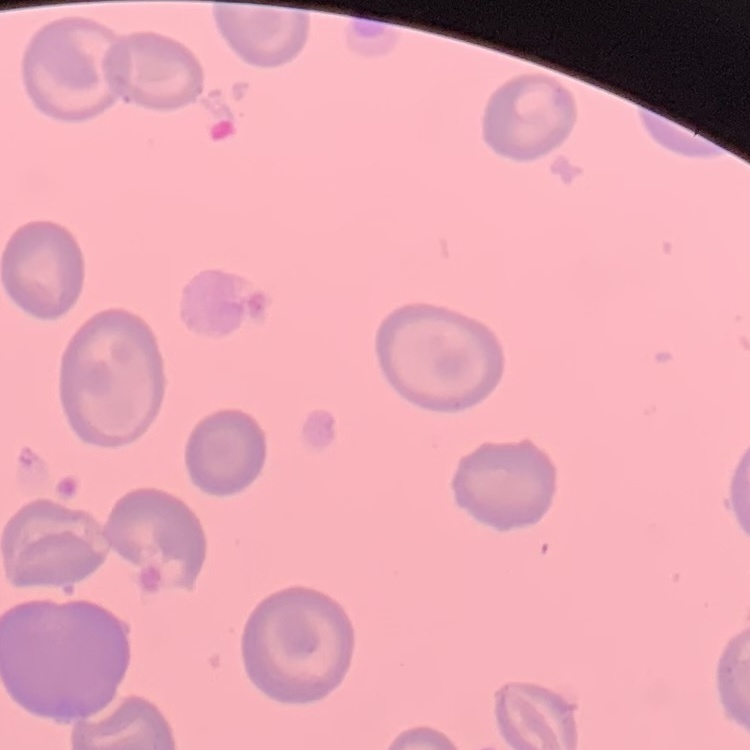
Summary:
  - Red blood cell morphology: no rouleaux formation
  - Stain: Field's or Giemsa
  - Preparation: thin blood film
  - Image type: one tile cut from a larger photomicrograph